Assess the morphology of the red blood cells.
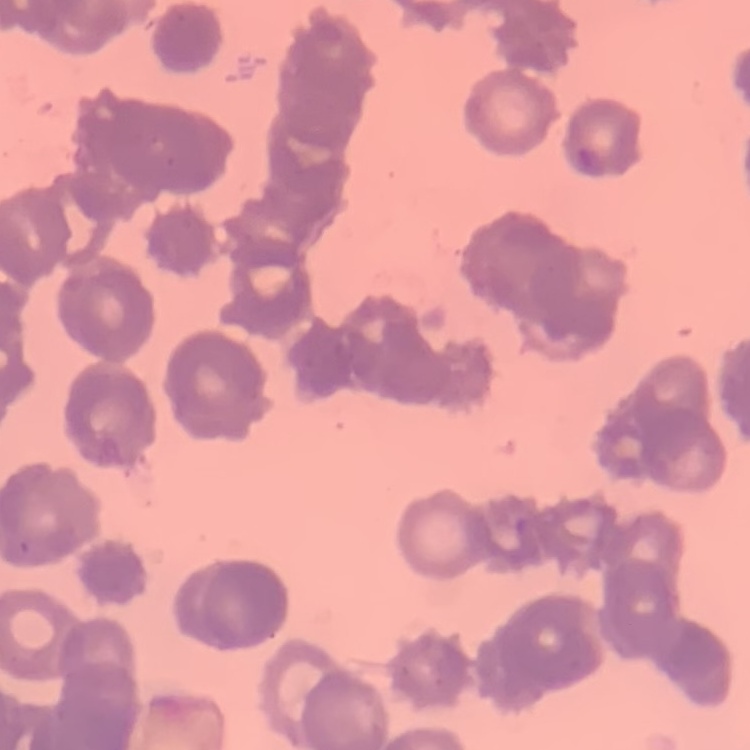

Rouleaux formation.

Thin blood smear. One tile cut from a larger photomicrograph. Stained with either Field's or Giemsa.